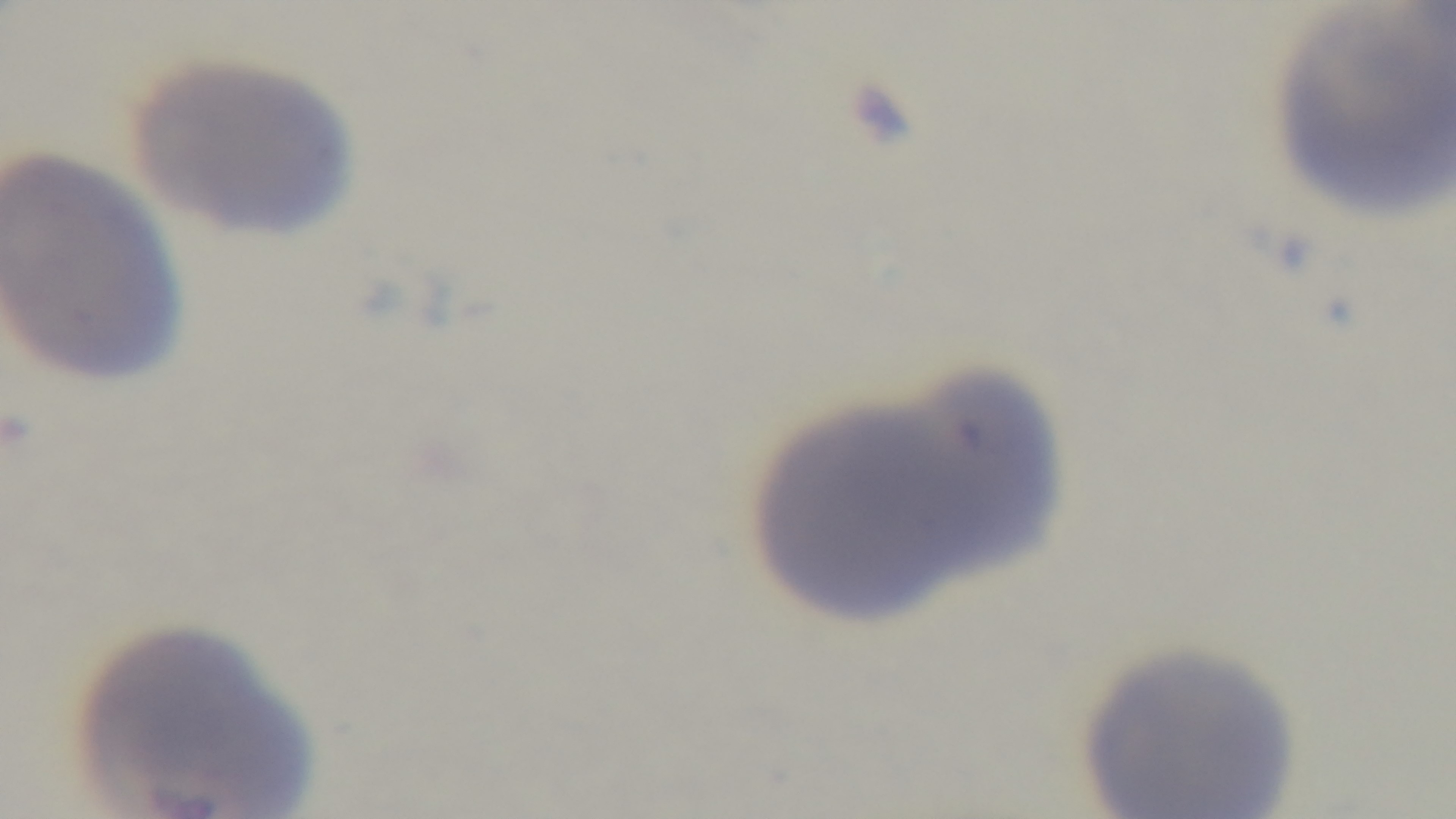

Oil-immersion objective, 100x. Single field of view. Preparation: thin. Malaria status: negative. Giemsa stain. Mounted 4K digital camera. Photomicrograph.